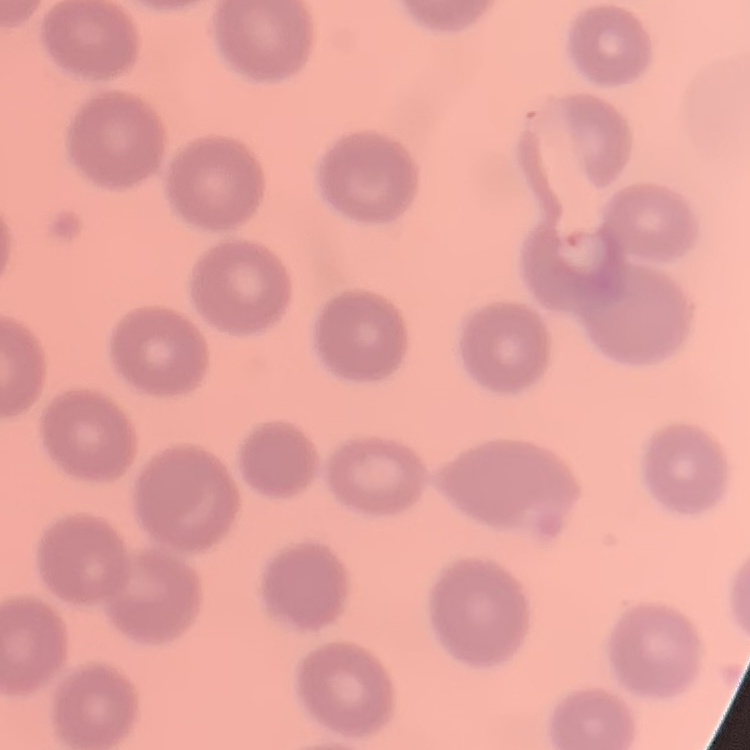 The red blood cells exhibit no rouleaux formation. One tile cut from a larger photomicrograph. Thin blood film. Field's or Giemsa stain.